Outline platelets.
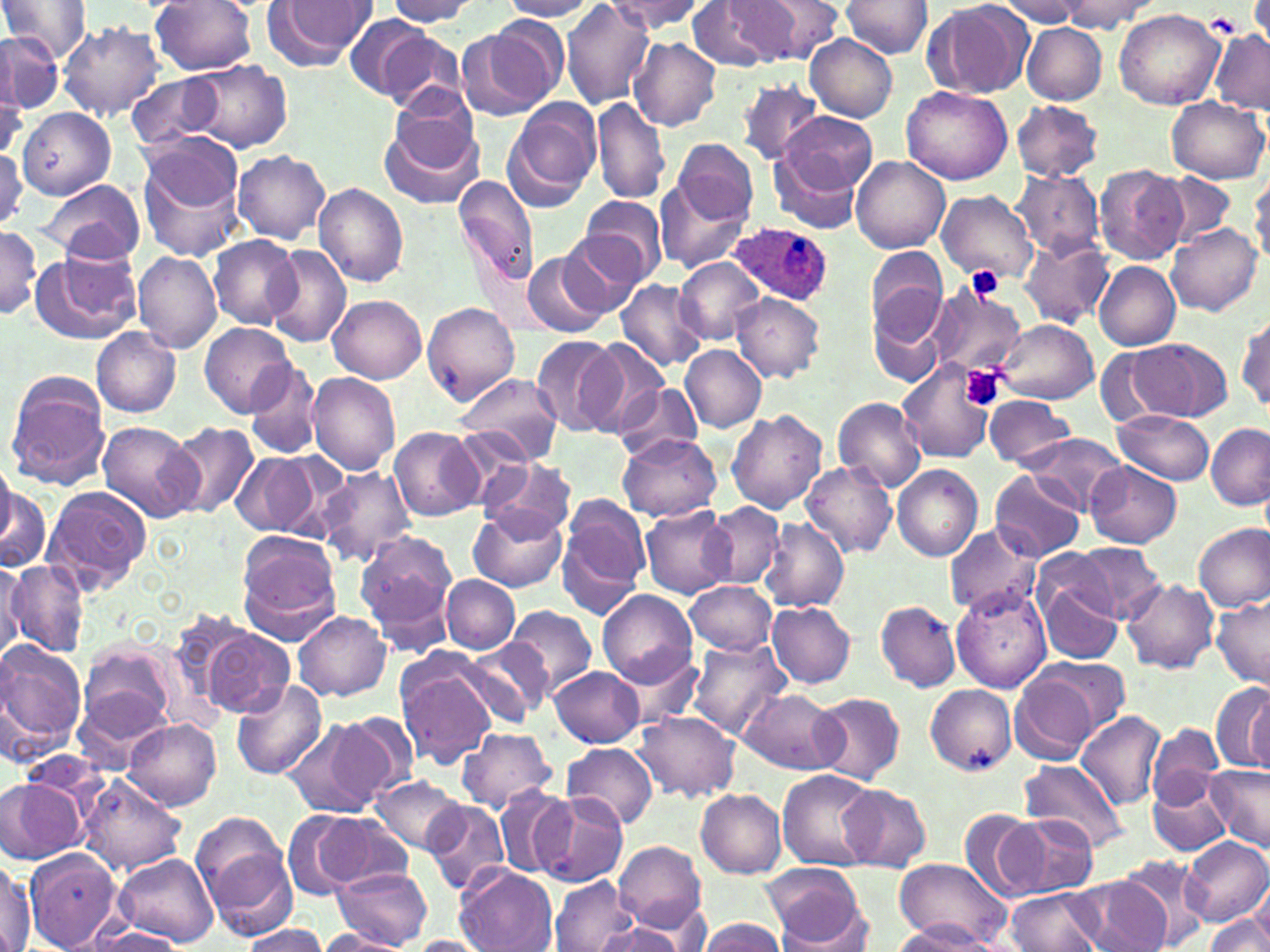

Approximate bounding boxes as named x1/y1/x2/y2 corners in pixels.
Platelets: (x1=1208, y1=12, x2=1241, y2=34), (x1=966, y1=267, x2=1006, y2=301), (x1=960, y1=365, x2=1007, y2=412).

slide-level diagnosis = Plasmodium ovale
image size = 1270×952 pixels
modality = light microscopy
magnification = 1000x
stain = May-Grünwald-Giemsa
preparation = thin blood film
Plasmodium ovale-infected red blood cell locations = approximate bounding boxes as named x1/y1/x2/y2 corners in pixels: (x1=728, y1=220, x2=834, y2=308)
field of view = single
uninfected red blood cell locations = approximate bounding boxes as named x1/y1/x2/y2 corners in pixels: (x1=0, y1=0, x2=92, y2=63), (x1=149, y1=0, x2=258, y2=74), (x1=386, y1=0, x2=481, y2=25), (x1=501, y1=0, x2=598, y2=21), (x1=606, y1=0, x2=707, y2=36), (x1=261, y1=1, x2=375, y2=70), (x1=560, y1=1, x2=657, y2=110), (x1=686, y1=1, x2=779, y2=70), (x1=726, y1=1, x2=833, y2=66), (x1=841, y1=1, x2=931, y2=58), (x1=997, y1=1, x2=1090, y2=27), (x1=1056, y1=1, x2=1151, y2=31), (x1=926, y1=4, x2=1026, y2=100), (x1=1114, y1=8, x2=1225, y2=109), (x1=346, y1=15, x2=433, y2=101), (x1=58, y1=21, x2=163, y2=121), (x1=462, y1=21, x2=565, y2=116), (x1=1022, y1=24, x2=1107, y2=103), (x1=373, y1=30, x2=471, y2=115), (x1=1210, y1=30, x2=1270, y2=114), (x1=0, y1=33, x2=61, y2=116), (x1=807, y1=35, x2=897, y2=121), (x1=628, y1=37, x2=721, y2=132), (x1=185, y1=59, x2=290, y2=152), (x1=127, y1=72, x2=224, y2=148), (x1=736, y1=79, x2=824, y2=165), (x1=901, y1=85, x2=1014, y2=185), (x1=0, y1=88, x2=26, y2=163), (x1=1166, y1=95, x2=1268, y2=182), (x1=591, y1=96, x2=670, y2=204), (x1=504, y1=98, x2=601, y2=209), (x1=1010, y1=101, x2=1104, y2=183), (x1=18, y1=108, x2=115, y2=200), (x1=379, y1=111, x2=485, y2=212), (x1=781, y1=111, x2=877, y2=192), (x1=674, y1=138, x2=758, y2=224), (x1=137, y1=145, x2=245, y2=260), (x1=0, y1=148, x2=26, y2=230), (x1=770, y1=148, x2=863, y2=234), (x1=234, y1=150, x2=331, y2=243), (x1=851, y1=156, x2=949, y2=252), (x1=1093, y1=165, x2=1188, y2=266), (x1=1152, y1=171, x2=1235, y2=250), (x1=1250, y1=171, x2=1270, y2=265), (x1=1010, y1=172, x2=1103, y2=256), (x1=454, y1=176, x2=539, y2=288), (x1=653, y1=179, x2=751, y2=274), (x1=34, y1=180, x2=146, y2=263), (x1=312, y1=182, x2=408, y2=287), (x1=936, y1=191, x2=1037, y2=283), (x1=576, y1=194, x2=667, y2=288), (x1=1168, y1=223, x2=1261, y2=317), (x1=0, y1=229, x2=42, y2=318), (x1=209, y1=235, x2=300, y2=331), (x1=558, y1=235, x2=646, y2=319), (x1=1020, y1=236, x2=1113, y2=329), (x1=264, y1=243, x2=350, y2=348), (x1=867, y1=249, x2=947, y2=346), (x1=31, y1=250, x2=141, y2=344), (x1=521, y1=250, x2=610, y2=339), (x1=133, y1=252, x2=222, y2=354), (x1=674, y1=259, x2=764, y2=343), (x1=1094, y1=261, x2=1180, y2=351), (x1=616, y1=279, x2=707, y2=373), (x1=924, y1=283, x2=1027, y2=382), (x1=730, y1=292, x2=826, y2=383), (x1=329, y1=295, x2=425, y2=384), (x1=867, y1=299, x2=947, y2=389), (x1=422, y1=303, x2=519, y2=403), (x1=1234, y1=311, x2=1269, y2=412), (x1=994, y1=318, x2=1099, y2=404), (x1=200, y1=322, x2=294, y2=417), (x1=93, y1=328, x2=181, y2=417), (x1=531, y1=334, x2=622, y2=435), (x1=579, y1=339, x2=669, y2=435), (x1=1128, y1=340, x2=1234, y2=421), (x1=680, y1=345, x2=769, y2=433), (x1=899, y1=361, x2=995, y2=463), (x1=246, y1=362, x2=320, y2=458), (x1=5, y1=371, x2=109, y2=490), (x1=307, y1=371, x2=401, y2=475), (x1=452, y1=372, x2=564, y2=467), (x1=615, y1=382, x2=705, y2=463), (x1=983, y1=394, x2=1077, y2=468), (x1=833, y1=397, x2=927, y2=493), (x1=726, y1=410, x2=828, y2=515), (x1=1116, y1=410, x2=1216, y2=485), (x1=163, y1=422, x2=260, y2=518), (x1=96, y1=423, x2=200, y2=521), (x1=1205, y1=423, x2=1270, y2=511), (x1=388, y1=426, x2=483, y2=521), (x1=617, y1=433, x2=723, y2=522), (x1=1023, y1=433, x2=1126, y2=514), (x1=231, y1=450, x2=326, y2=539), (x1=479, y1=456, x2=576, y2=538), (x1=1084, y1=460, x2=1181, y2=547), (x1=801, y1=461, x2=897, y2=560), (x1=892, y1=463, x2=982, y2=561), (x1=0, y1=465, x2=23, y2=559), (x1=315, y1=466, x2=417, y2=566), (x1=991, y1=470, x2=1085, y2=562), (x1=0, y1=478, x2=51, y2=576), (x1=40, y1=487, x2=151, y2=592), (x1=558, y1=498, x2=649, y2=617), (x1=640, y1=503, x2=737, y2=597), (x1=699, y1=504, x2=786, y2=590), (x1=468, y1=506, x2=568, y2=593), (x1=759, y1=518, x2=849, y2=611), (x1=944, y1=523, x2=1040, y2=618), (x1=1195, y1=523, x2=1270, y2=613), (x1=356, y1=532, x2=457, y2=647), (x1=235, y1=533, x2=343, y2=642), (x1=1069, y1=542, x2=1167, y2=624), (x1=0, y1=559, x2=24, y2=659), (x1=6, y1=560, x2=92, y2=657), (x1=1037, y1=566, x2=1125, y2=666), (x1=441, y1=575, x2=520, y2=654), (x1=1122, y1=579, x2=1217, y2=675), (x1=686, y1=581, x2=777, y2=654), (x1=953, y1=586, x2=1052, y2=693), (x1=597, y1=590, x2=697, y2=688), (x1=1211, y1=598, x2=1269, y2=686), (x1=875, y1=600, x2=960, y2=693), (x1=766, y1=602, x2=857, y2=688), (x1=506, y1=604, x2=596, y2=698), (x1=294, y1=611, x2=390, y2=701), (x1=197, y1=622, x2=296, y2=718), (x1=459, y1=636, x2=552, y2=726), (x1=687, y1=637, x2=792, y2=739), (x1=0, y1=639, x2=87, y2=750), (x1=76, y1=641, x2=179, y2=748), (x1=618, y1=650, x2=703, y2=733), (x1=395, y1=657, x2=498, y2=767), (x1=1039, y1=657, x2=1131, y2=731), (x1=551, y1=666, x2=646, y2=747), (x1=1012, y1=673, x2=1101, y2=766), (x1=230, y1=680, x2=328, y2=779), (x1=1213, y1=681, x2=1270, y2=774), (x1=925, y1=685, x2=1016, y2=774), (x1=737, y1=688, x2=844, y2=775), (x1=808, y1=692, x2=904, y2=785), (x1=634, y1=710, x2=740, y2=801), (x1=1076, y1=711, x2=1166, y2=811), (x1=333, y1=712, x2=418, y2=800), (x1=123, y1=718, x2=221, y2=809), (x1=281, y1=718, x2=390, y2=818), (x1=1148, y1=724, x2=1223, y2=808), (x1=455, y1=727, x2=558, y2=814), (x1=562, y1=742, x2=658, y2=829), (x1=1020, y1=759, x2=1128, y2=852), (x1=1205, y1=765, x2=1270, y2=853), (x1=777, y1=769, x2=878, y2=871), (x1=1147, y1=771, x2=1231, y2=858), (x1=77, y1=773, x2=187, y2=875), (x1=372, y1=775, x2=467, y2=857), (x1=1, y1=778, x2=86, y2=864), (x1=494, y1=783, x2=575, y2=879), (x1=838, y1=785, x2=931, y2=871), (x1=696, y1=789, x2=786, y2=877), (x1=533, y1=793, x2=627, y2=886), (x1=423, y1=799, x2=511, y2=895), (x1=958, y1=809, x2=1048, y2=902), (x1=283, y1=810, x2=390, y2=900), (x1=1009, y1=812, x2=1103, y2=895), (x1=193, y1=815, x2=296, y2=938), (x1=1179, y1=837, x2=1270, y2=926), (x1=613, y1=841, x2=706, y2=935), (x1=25, y1=848, x2=122, y2=950), (x1=113, y1=852, x2=220, y2=947), (x1=1116, y1=852, x2=1215, y2=950), (x1=0, y1=855, x2=34, y2=952), (x1=894, y1=858, x2=1013, y2=947), (x1=763, y1=864, x2=870, y2=947), (x1=333, y1=866, x2=432, y2=949), (x1=455, y1=866, x2=558, y2=952), (x1=551, y1=874, x2=640, y2=952), (x1=1070, y1=876, x2=1171, y2=952), (x1=1006, y1=887, x2=1104, y2=952), (x1=1243, y1=887, x2=1270, y2=946), (x1=1204, y1=913, x2=1269, y2=952), (x1=696, y1=917, x2=788, y2=952), (x1=895, y1=921, x2=1000, y2=951), (x1=236, y1=925, x2=330, y2=952), (x1=593, y1=925, x2=686, y2=952), (x1=86, y1=926, x2=187, y2=951), (x1=316, y1=929, x2=409, y2=951), (x1=407, y1=935, x2=492, y2=952)